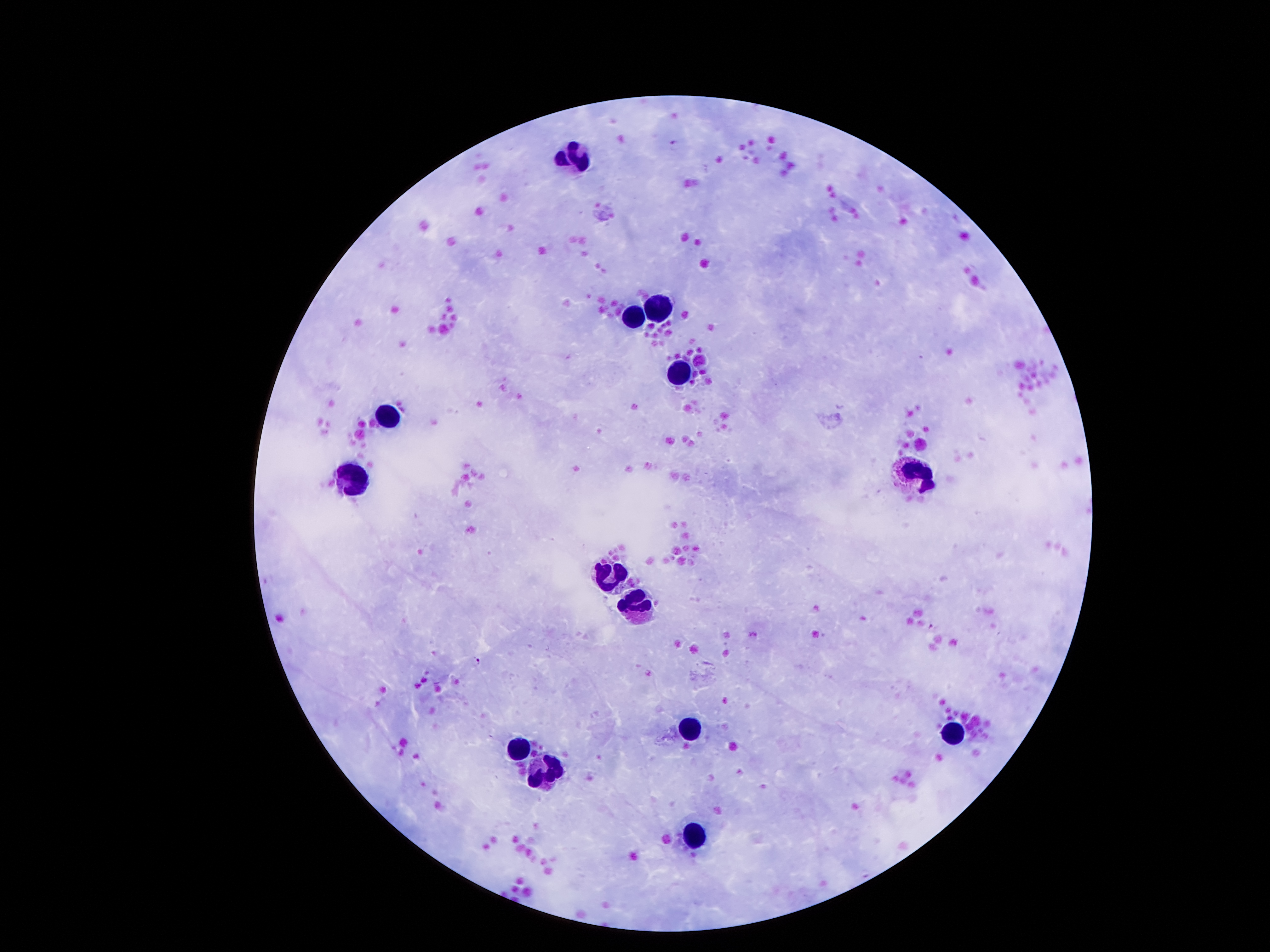
Approximate centers as [x, y] in pixels. Plasmodium parasite locations: [673, 144], [932, 625], [476, 661]. Leukocyte locations: [576, 158], [658, 308], [634, 316], [685, 374], [386, 413], [918, 472], [357, 483], [615, 572], [636, 603], [691, 726], [949, 731], [517, 747], [541, 774], [695, 839]. Image is 1270×952 pixels. 100x magnification. Photographed through the microscope eyepiece with a smartphone camera. Patient malaria status: positive for Plasmodium falciparum. One field from this slide. Thick peripheral-blood smear. Giemsa-stained preparation.